Locate and identify every blood parasite.
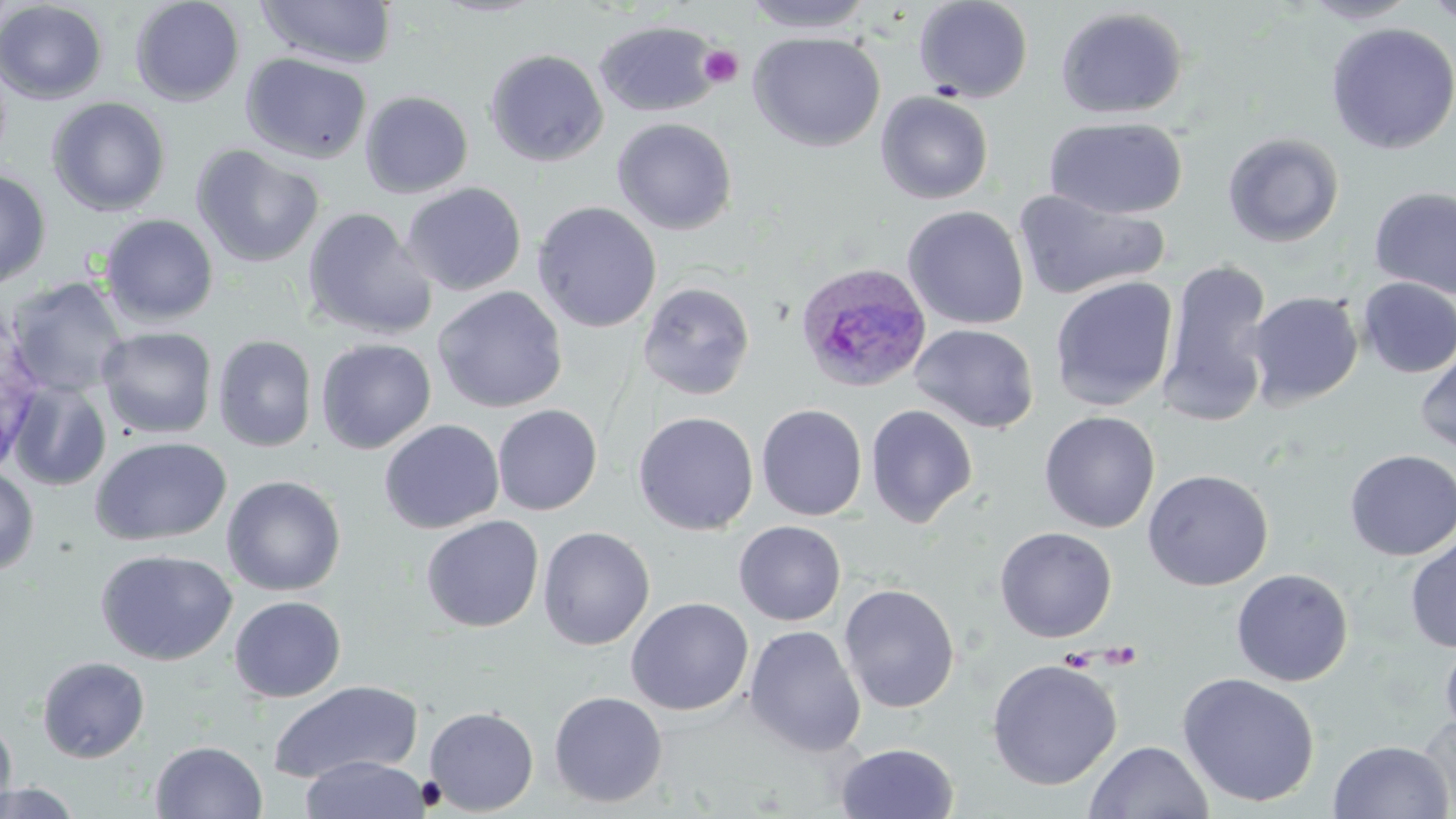
Approximate bounding boxes as (x1,y1)-(x2,y2) corner pairs in pixels.
Plasmodium ovale-infected red blood cells: (795,261)-(933,394).
No Plasmodium falciparum, Plasmodium malariae, Plasmodium vivax, Babesia divergens, or Trypanosoma brucei observed.

Platelet locations: (698,45)-(744,88). Uninfected red blood cell locations: (129,0)-(245,107), (256,0)-(397,69), (430,0)-(549,18), (741,0)-(876,33), (913,0)-(1033,103), (1299,0)-(1422,25), (1420,0)-(1456,27), (0,1)-(108,105), (1055,6)-(1189,120), (594,20)-(720,117), (1325,22)-(1456,154), (748,31)-(886,152), (484,48)-(609,167), (241,52)-(373,164), (360,90)-(473,199), (876,91)-(994,204), (46,97)-(171,217), (1046,116)-(1188,220), (612,117)-(737,235), (1222,132)-(1345,248), (190,144)-(324,268), (0,169)-(52,290), (401,182)-(527,296), (1369,187)-(1456,299), (1012,189)-(1169,301), (532,201)-(662,333), (902,205)-(1029,330), (301,207)-(438,341), (98,214)-(219,326), (1160,256)-(1274,426), (1049,276)-(1179,412), (4,277)-(128,398), (1357,277)-(1456,378), (637,281)-(756,400), (433,286)-(567,413), (1247,291)-(1363,409), (909,323)-(1040,434), (97,326)-(217,439), (212,334)-(317,452), (316,338)-(436,454), (1415,346)-(1456,455), (8,381)-(112,491), (756,403)-(868,521), (492,404)-(602,515), (866,405)-(978,528), (632,411)-(759,535), (1039,411)-(1160,534), (379,419)-(504,535), (89,436)-(232,547), (1344,449)-(1456,561), (0,466)-(39,578), (1142,468)-(1274,591), (222,475)-(346,596), (421,515)-(544,632), (734,521)-(846,625), (537,526)-(655,651), (994,526)-(1117,643), (1405,534)-(1456,653), (95,548)-(237,666), (1231,568)-(1353,687), (838,583)-(960,713), (228,595)-(346,702), (626,597)-(754,716), (744,625)-(866,757), (1440,635)-(1456,742), (37,656)-(150,763), (985,659)-(1123,790), (1177,672)-(1321,809), (267,680)-(424,784), (548,690)-(668,808), (424,706)-(539,815), (1415,712)-(1455,813), (0,716)-(17,812), (1327,739)-(1454,819), (1085,740)-(1213,819), (150,741)-(267,819), (835,742)-(959,819), (299,755)-(431,819), (1,782)-(83,818). Slide-level diagnosis: Plasmodium ovale. 1000x magnification. Light microscopy. Image is 1456×819 pixels. May-Grünwald-Giemsa stain. One field of a larger specimen. Thin blood film.